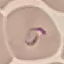

result = malaria parasites identified
stain = Giemsa
preparation = thin smear
image type = cell patch, automatically extracted from a larger field of view and resized to 64 × 64 pixels
capture = smartphone through the microscope eyepiece